Assess this cell for malaria.
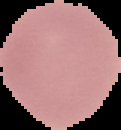
Uninfected.

image size = 121×130 pixels
image type = segmented cell region on a black background
preparation = thin blood film